Classify this cell by malaria status.
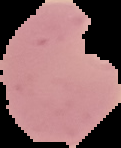
It is parasitized.

Summary:
  - Image type: segmented cell region on a black background
  - Image size: 121×148 pixels
  - Preparation: thin blood smear